Classify this cell by malaria status.
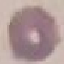
Uninfected.

capture = smartphone camera at the microscope eyepiece
stain = Giemsa
image type = automatically extracted cell patch, resized to 64 × 64 pixels
preparation = thin blood film